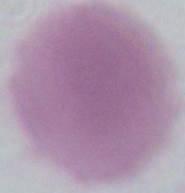

Summary:
  - Magnification: 1000x
  - Identification: red blood cell
  - Modality: micrograph